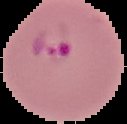

preparation = thin blood smear
image size = 127×124 pixels
result = malaria parasites detected
image type = cell region segmented out of the field of view; surrounding area masked to black